Name the parasite shown.
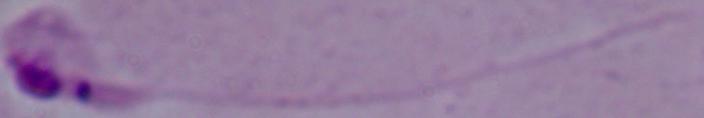

This is Leishmania.

Summary:
  - Magnification: 1000x
  - Modality: micrograph